Report the malaria status of this cell.
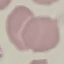

It is uninfected.

stain = Giemsa
image type = automatically extracted cell patch, resized to 64 × 64 pixels
capture = smartphone through the microscope eyepiece
preparation = thin blood smear